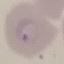
result = malaria parasites identified
stain = Giemsa
preparation = thin blood film
capture = smartphone camera at the microscope eyepiece
image type = cell patch, automatically extracted from a larger field of view and resized to 64 × 64 pixels